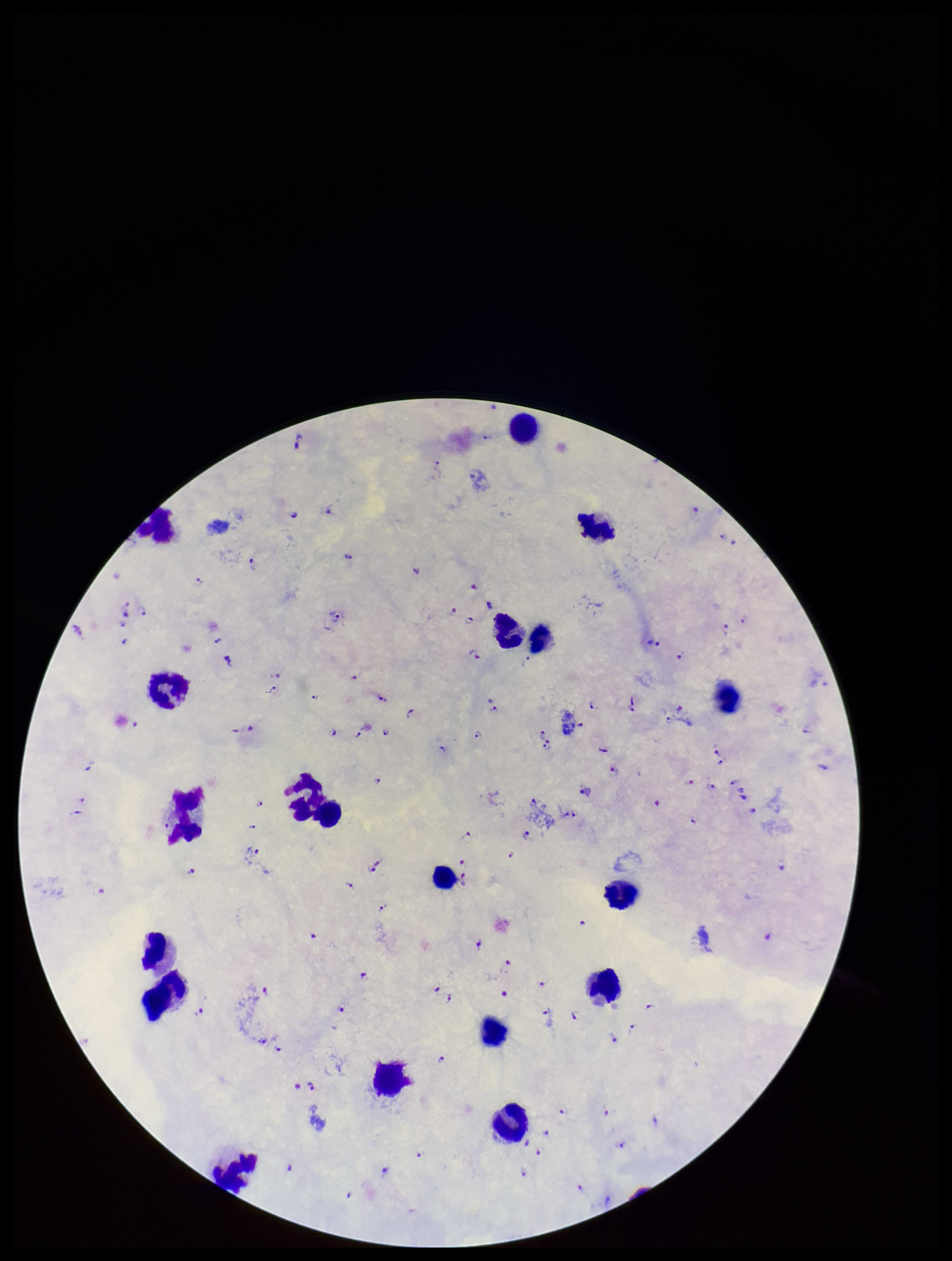
Summary:
  - Capture: smartphone photograph through the microscope eyepiece
  - Preparation: thick smear
  - Patient malaria status: infected
  - Stain: Giemsa
  - Image size: 952×1261 pixels
  - Field of view: single
  - Plasmodium parasites: identified
  - Species reported for this patient: Plasmodium falciparum
  - Parasite count: 108
  - Leukocyte count: 18